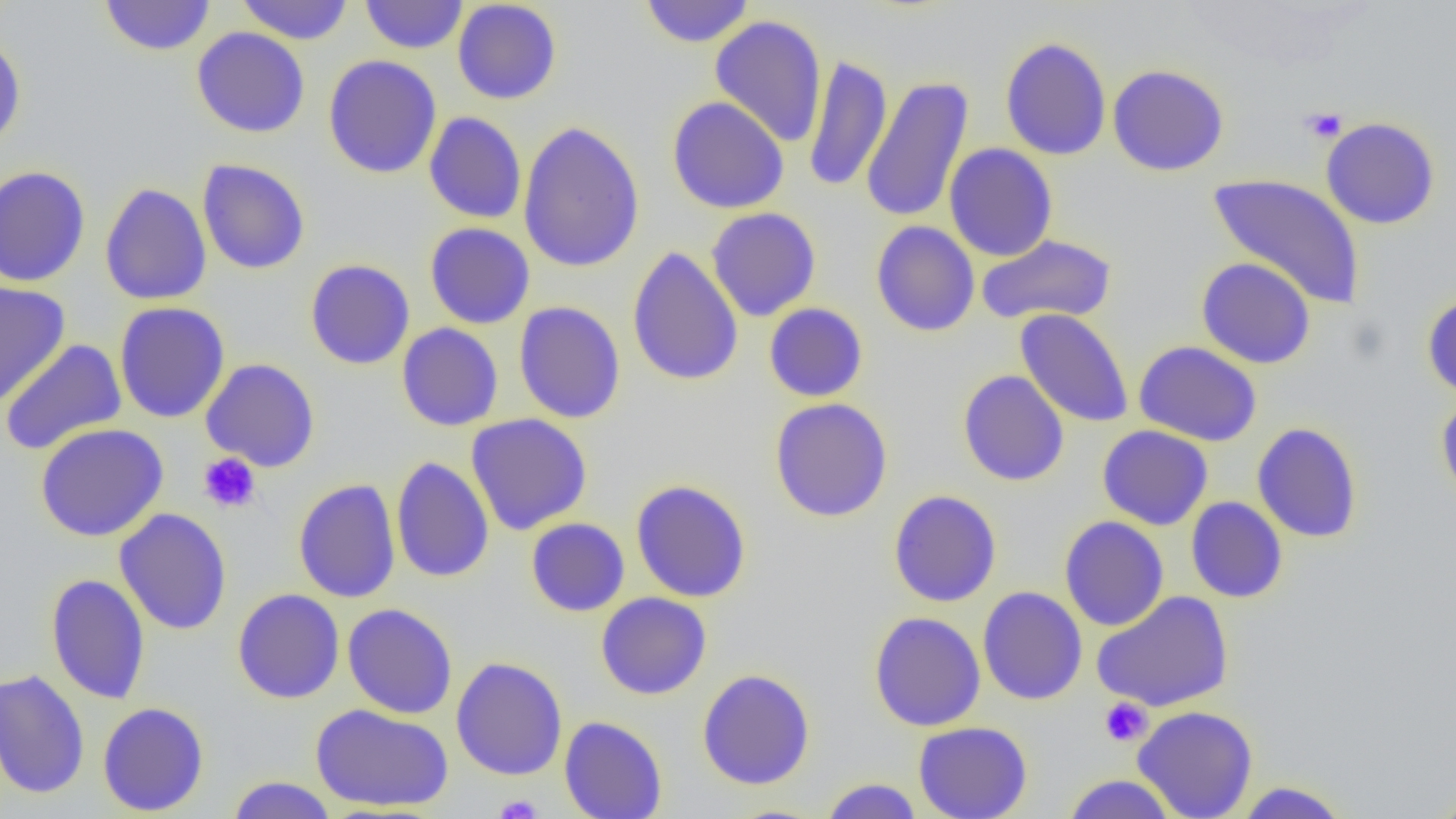
Approximate bounding boxes as (x1,y1)-(x2,y2) corner pairs in pixels. Platelet locations: (1300,107)-(1347,143), (197,452)-(261,513), (1099,697)-(1153,746), (493,795)-(544,819). Uninfected red blood cell locations: (99,0)-(216,56), (235,0)-(355,45), (360,0)-(468,54), (452,1)-(562,104), (639,1)-(755,48), (710,15)-(827,148), (192,27)-(310,138), (0,33)-(27,152), (999,36)-(1112,161), (802,54)-(892,193), (323,55)-(442,179), (1107,64)-(1229,176), (861,76)-(975,224), (667,96)-(790,214), (424,111)-(527,224), (1321,117)-(1440,229), (518,120)-(646,273), (944,143)-(1058,261), (196,159)-(310,275), (0,165)-(91,287), (1208,173)-(1367,309), (99,182)-(212,306), (705,207)-(821,320), (871,221)-(980,337), (424,222)-(535,329), (977,234)-(1116,326), (627,245)-(743,387), (1196,257)-(1316,369), (305,259)-(415,370), (0,280)-(70,408), (1422,292)-(1456,401), (114,301)-(230,423), (514,301)-(626,424), (763,303)-(868,402), (1015,309)-(1134,428), (396,323)-(503,431), (1,339)-(127,456), (1133,341)-(1262,447), (200,358)-(320,472), (957,370)-(1069,486), (1435,391)-(1456,509), (770,398)-(893,522), (466,413)-(593,535), (1251,422)-(1363,543), (35,423)-(169,542), (1097,425)-(1213,530), (391,456)-(494,583), (293,479)-(401,603), (630,479)-(751,602), (888,489)-(1002,607), (1186,497)-(1288,603), (115,508)-(231,635), (1059,516)-(1169,631), (526,518)-(630,617), (46,574)-(150,704), (977,586)-(1087,705), (233,588)-(345,704), (1091,591)-(1234,712), (596,592)-(711,700), (342,603)-(458,719), (868,611)-(986,731), (451,656)-(568,781), (0,669)-(91,799), (697,669)-(815,790), (97,702)-(209,816), (310,703)-(454,812), (1132,705)-(1259,819), (559,716)-(667,819), (913,721)-(1032,818), (1061,774)-(1179,819), (226,776)-(338,819), (819,778)-(924,818), (1231,781)-(1354,818), (1428,786)-(1456,819). Slide-level diagnosis: no evidence of blood parasites. Single field of view. Optical microscopy. Thin blood smear. Image is 1456×819 pixels. 1000x magnification.